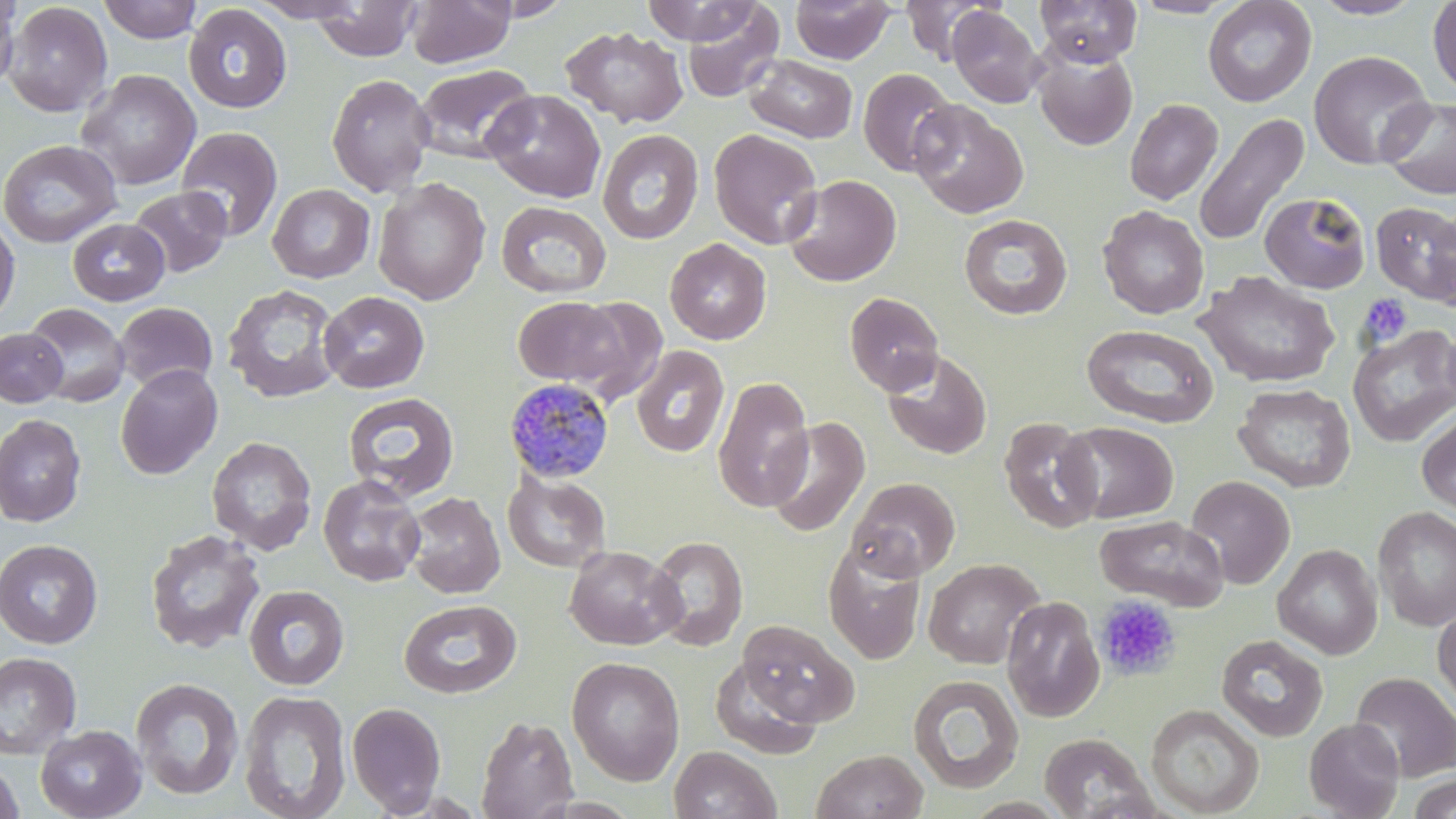

{
  "slide_level_diagnosis": "Plasmodium malariae",
  "stain": "May-Grünwald-Giemsa",
  "magnification": "1000x",
  "platelet_locations_subset": "approximate bounding boxes as [x1, y1, x2, y2] in pixels: [1358, 293, 1411, 347]",
  "preparation": "thin blood film",
  "plasmodium_malariae_infected_red_blood_cell_locations": "approximate bounding boxes as [x1, y1, x2, y2] in pixels: [503, 378, 615, 484]",
  "image_size": "1456×819 pixels",
  "modality": "optical microscopy",
  "field_of_view": "single",
  "uninfected_red_blood_cell_locations_subset": "approximate bounding boxes as [x1, y1, x2, y2] in pixels: [0, 0, 21, 95], [97, 0, 203, 44], [251, 0, 365, 22], [407, 0, 516, 68], [474, 0, 575, 21], [641, 0, 762, 45], [790, 0, 895, 65], [1035, 0, 1142, 67], [1203, 0, 1317, 107], [1309, 0, 1426, 20], [1427, 0, 1456, 98], [309, 1, 422, 61], [680, 1, 785, 103], [901, 1, 996, 64], [1131, 1, 1240, 18], [3, 2, 112, 117], [184, 4, 293, 114], [947, 5, 1045, 108], [561, 26, 689, 128], [1033, 49, 1138, 152], [1309, 51, 1434, 169], [745, 54, 858, 143], [413, 63, 537, 164], [858, 68, 959, 177], [76, 70, 201, 190], [326, 73, 435, 196], [483, 89, 606, 203], [1379, 97, 1456, 199], [1124, 98, 1223, 205], [909, 100, 1028, 219], [1195, 113, 1309, 246], [176, 126, 283, 241], [597, 128, 704, 245], [709, 128, 823, 249], [0, 139, 122, 248], [784, 174, 902, 287], [372, 177, 491, 306], [267, 184, 375, 283], [128, 186, 232, 277], [1259, 192, 1371, 293], [496, 200, 612, 299], [1371, 201, 1456, 307], [1098, 206, 1209, 319], [959, 214, 1072, 319], [0, 216, 20, 326], [67, 218, 170, 306], [664, 238, 771, 345], [1196, 271, 1340, 389], [222, 283, 343, 404], [319, 291, 430, 393], [844, 292, 944, 396], [513, 296, 626, 390], [565, 298, 669, 403], [24, 302, 130, 407], [113, 302, 218, 393], [1082, 324, 1218, 428], [1347, 324, 1456, 447], [0, 328, 67, 407], [631, 345, 729, 458], [883, 350, 992, 459], [115, 364, 223, 480], [712, 375, 814, 512], [1233, 383, 1356, 493], [343, 392, 460, 502], [1417, 412, 1456, 515], [0, 414, 86, 526], [763, 416, 870, 537], [999, 417, 1103, 533], [1060, 421, 1179, 523], [206, 436, 317, 555], [502, 470, 611, 573], [318, 474, 427, 587], [1185, 475, 1295, 590], [848, 477, 960, 580], [404, 491, 506, 599], [1373, 506, 1456, 631], [1094, 515, 1229, 610], [145, 529, 266, 655], [647, 535, 748, 651], [0, 539, 103, 649], [823, 539, 928, 665], [1272, 543, 1383, 659], [564, 545, 684, 650], [923, 558, 1045, 669], [244, 584, 350, 690], [1001, 596, 1105, 722], [399, 599, 522, 698], [1432, 603, 1456, 718], [737, 620, 859, 727], [1217, 635, 1327, 741], [0, 651, 82, 758], [709, 655, 823, 759], [566, 656, 685, 785], [1349, 671, 1456, 782], [908, 674, 1024, 793], [131, 677, 244, 800], [239, 689, 351, 819], [346, 701, 447, 816], [1146, 703, 1265, 817], [476, 715, 578, 819], [1304, 717, 1404, 818], [35, 724, 146, 819], [1039, 733, 1158, 818], [669, 746, 781, 819], [812, 749, 928, 819], [0, 758, 24, 819], [1407, 774, 1456, 819]"
}